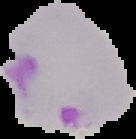

malaria_status: parasitized
image_type: cell region segmented out of the field of view; surrounding area masked to black
preparation: thin blood film
image_size: 136×139 pixels